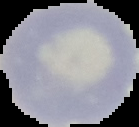
{
  "image_type": "segmented cell region with the area outside set to black",
  "image_size": "139×127 pixels",
  "preparation": "thin blood smear",
  "malaria_status": "uninfected"
}